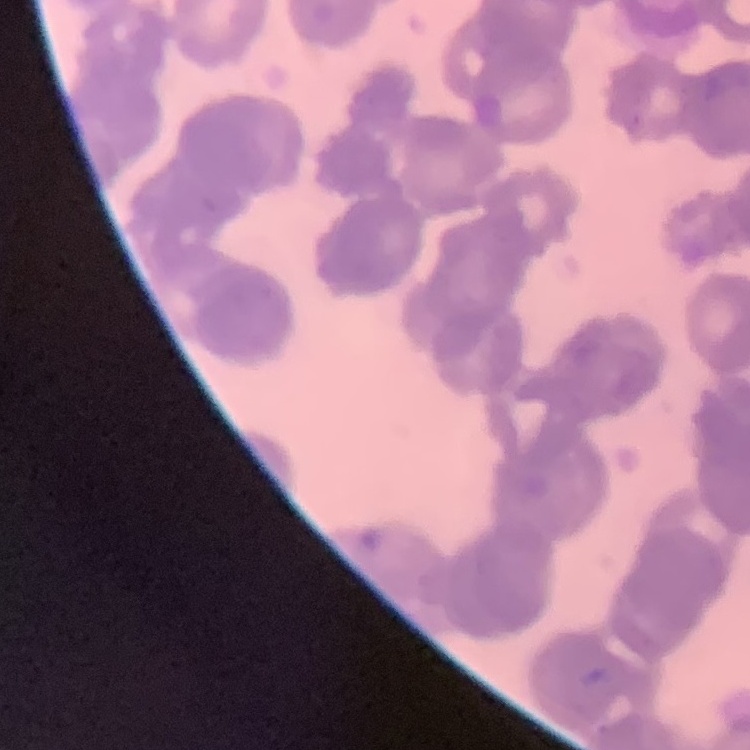

red_blood_cell_morphology: rouleaux formation
preparation: thin peripheral smear
stain: Field's or Giemsa
image_type: square crop of a larger photomicrograph